Name the blood parasite species.
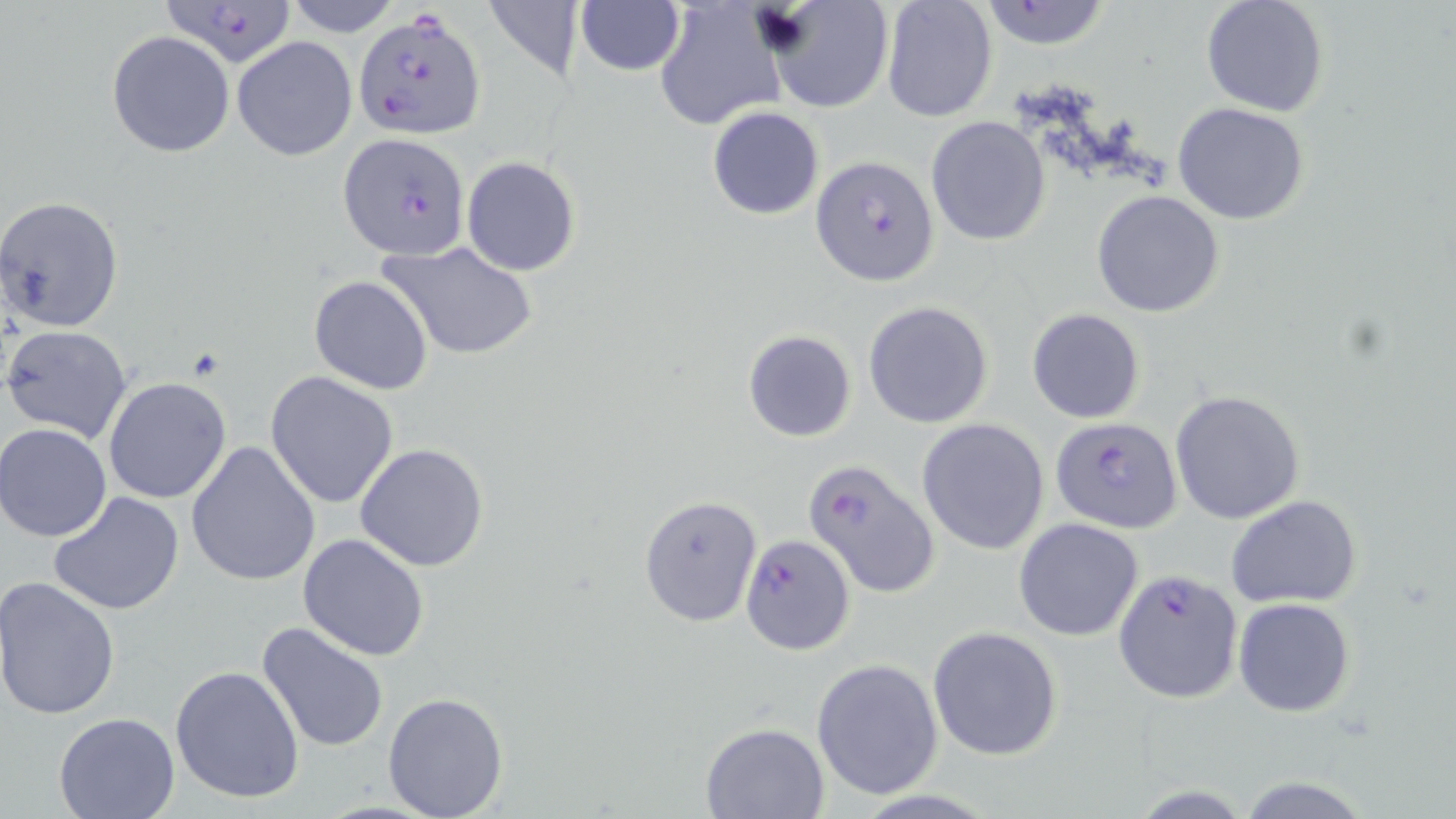
Plasmodium falciparum.

Approximate bounding boxes as named x1/y1/x2/y2 corners in pixels. Plasmodium falciparum-infected red blood cell locations: (x1=160, y1=1, x2=295, y2=65), (x1=355, y1=9, x2=487, y2=141), (x1=339, y1=132, x2=470, y2=261), (x1=810, y1=155, x2=939, y2=286), (x1=1051, y1=415, x2=1182, y2=530), (x1=804, y1=459, x2=940, y2=597), (x1=740, y1=533, x2=856, y2=655), (x1=1114, y1=569, x2=1244, y2=703). Uninfected red blood cell locations: (x1=285, y1=0, x2=401, y2=38), (x1=481, y1=0, x2=584, y2=78), (x1=654, y1=0, x2=786, y2=131), (x1=1200, y1=0, x2=1330, y2=117), (x1=766, y1=1, x2=893, y2=113), (x1=880, y1=1, x2=997, y2=121), (x1=974, y1=1, x2=1116, y2=50), (x1=575, y1=2, x2=686, y2=76), (x1=108, y1=32, x2=234, y2=157), (x1=233, y1=36, x2=358, y2=161), (x1=1172, y1=103, x2=1312, y2=225), (x1=708, y1=106, x2=824, y2=220), (x1=925, y1=116, x2=1052, y2=247), (x1=461, y1=157, x2=581, y2=276), (x1=1092, y1=190, x2=1225, y2=317), (x1=1, y1=196, x2=126, y2=333), (x1=377, y1=240, x2=539, y2=360), (x1=309, y1=274, x2=434, y2=394), (x1=864, y1=301, x2=994, y2=429), (x1=1026, y1=307, x2=1145, y2=423), (x1=3, y1=325, x2=133, y2=443), (x1=743, y1=330, x2=856, y2=442), (x1=265, y1=371, x2=400, y2=508), (x1=103, y1=376, x2=232, y2=504), (x1=1170, y1=389, x2=1305, y2=524), (x1=917, y1=418, x2=1050, y2=555), (x1=1, y1=422, x2=112, y2=541), (x1=186, y1=441, x2=320, y2=585), (x1=357, y1=443, x2=489, y2=570), (x1=48, y1=491, x2=187, y2=614), (x1=639, y1=494, x2=762, y2=626), (x1=1226, y1=494, x2=1362, y2=608), (x1=1013, y1=517, x2=1145, y2=641), (x1=298, y1=533, x2=431, y2=660), (x1=0, y1=577, x2=121, y2=721), (x1=1233, y1=597, x2=1357, y2=717), (x1=256, y1=621, x2=390, y2=753), (x1=926, y1=626, x2=1063, y2=761), (x1=811, y1=658, x2=944, y2=800), (x1=169, y1=664, x2=306, y2=804), (x1=383, y1=691, x2=508, y2=817), (x1=54, y1=710, x2=180, y2=818), (x1=699, y1=722, x2=830, y2=818). One field of a larger specimen. Thin blood film. May-Grünwald-Giemsa stain. 1000x magnification. Image is 1456×819 pixels. Light microscopy.